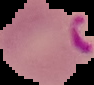

image size = 94×85 pixels
image type = segmented cell region on a black background
preparation = thin blood film
result = Plasmodium parasites detected